Find each white blood cell.
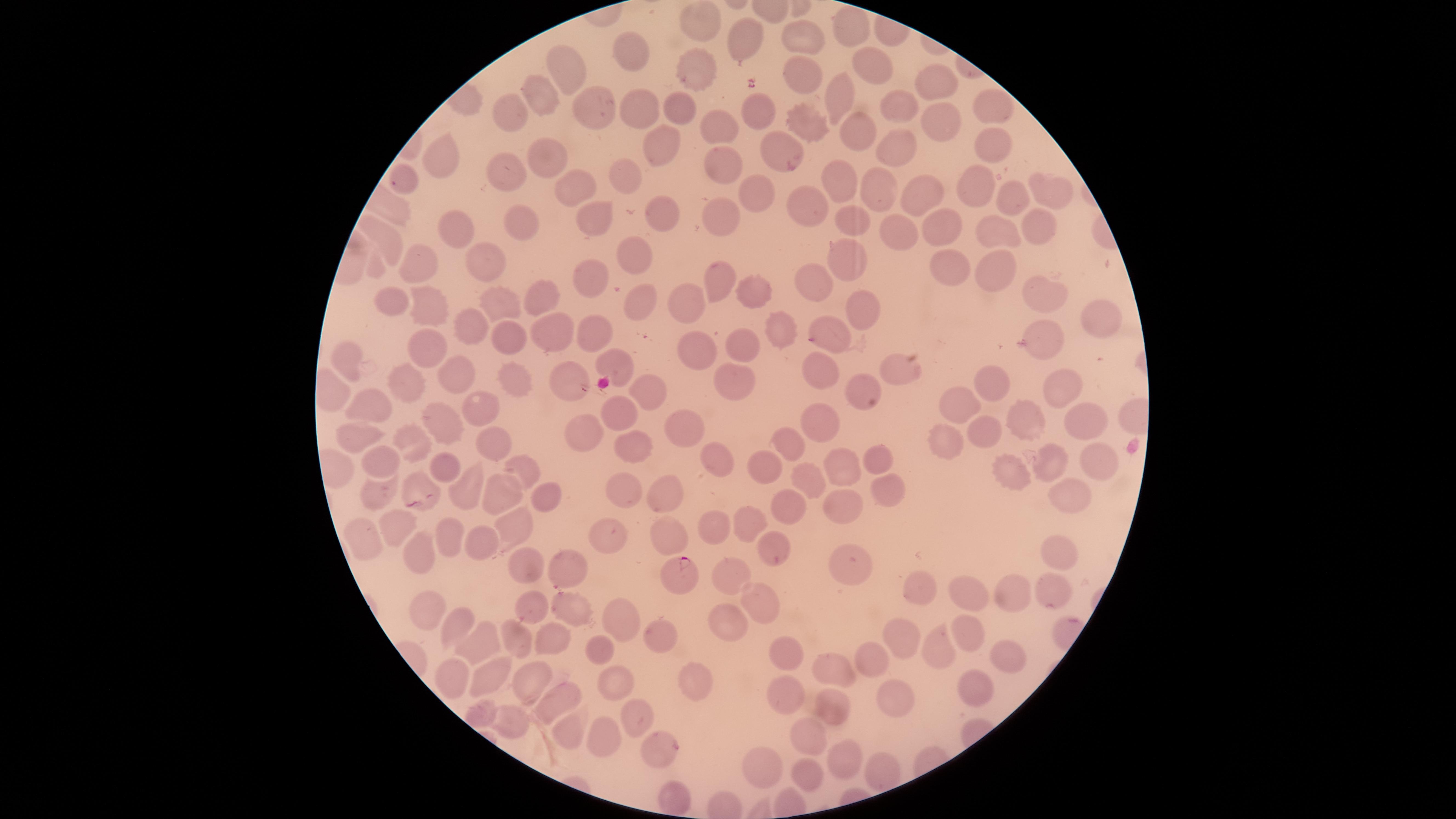

No white blood cells identified.

Approximate marker points as {x, y} in pixels.
Summary:
  - Parasitized red blood cells: {679, 573}
  - Uninfected red blood cells: {704, 20}, {856, 27}, {745, 38}, {808, 40}, {634, 46}, {871, 68}, {566, 69}, {696, 74}, {800, 79}, {940, 79}, {835, 97}, {541, 100}, {985, 104}, {637, 106}, {902, 106}, {663, 108}, {756, 109}, {595, 110}, {512, 111}, {942, 123}, {804, 124}, {854, 126}, {720, 128}, {987, 140}, {655, 146}, {779, 148}, {899, 152}, {547, 159}, {447, 160}, {506, 170}, {733, 170}, {841, 177}, {405, 181}, {620, 181}, {1050, 184}, {571, 186}, {876, 187}, {980, 187}, {913, 191}, {1013, 194}, {749, 195}, {806, 208}, {595, 209}, {656, 216}, {528, 221}, {720, 223}, {850, 223}, {1034, 223}, {455, 228}, {946, 229}, {907, 233}, {999, 233}, {385, 235}, {637, 249}, {477, 257}, {845, 262}, {951, 263}, {414, 264}, {991, 273}, {592, 275}, {716, 276}, {811, 281}, {755, 292}, {1044, 294}, {502, 296}, {549, 296}, {640, 299}, {397, 301}, {424, 303}, {688, 304}, {864, 309}, {1100, 318}, {776, 321}, {464, 327}, {596, 330}, {550, 333}, {1044, 333}, {837, 334}, {503, 336}, {704, 345}, {433, 346}, {744, 348}, {350, 361}, {616, 361}, {901, 368}, {821, 372}, {461, 375}, {736, 378}, {404, 381}, {512, 381}, {567, 381}, {996, 386}, {649, 388}, {860, 388}, {1061, 388}, {960, 404}, {377, 407}, {482, 411}, {624, 411}, {445, 416}, {822, 417}, {1025, 417}, {1088, 420}, {690, 423}, {586, 426}, {362, 436}, {492, 442}, {412, 444}, {633, 445}, {787, 445}, {716, 456}, {876, 456}, {1096, 463}, {382, 464}, {1047, 466}, {443, 468}, {521, 469}, {761, 470}, {842, 471}, {1013, 473}, {806, 484}, {414, 486}, {625, 489}, {887, 489}, {471, 490}, {672, 493}, {378, 496}, {1067, 498}, {501, 499}, {544, 499}, {842, 508}, {782, 509}, {750, 523}, {399, 525}, {711, 526}, {514, 530}, {610, 531}, {445, 534}, {668, 538}, {360, 541}, {480, 542}, {774, 552}, {420, 553}, {1049, 554}, {565, 563}, {518, 566}, {846, 570}, {733, 573}, {917, 588}, {972, 590}, {1052, 596}, {1016, 599}, {570, 601}, {759, 604}, {530, 605}, {429, 611}, {614, 618}, {729, 624}, {456, 625}, {968, 630}, {661, 633}, {903, 634}, {547, 636}, {482, 639}, {516, 645}, {937, 647}, {601, 649}, {786, 649}, {1010, 656}, {839, 667}, {878, 668}, {452, 678}, {489, 678}, {528, 679}, {697, 682}, {614, 684}, {978, 685}, {785, 694}, {558, 698}, {897, 701}, {831, 707}, {478, 714}, {639, 716}, {509, 721}, {603, 729}, {566, 735}, {809, 737}, {665, 752}, {841, 755}, {878, 768}, {763, 770}, {808, 772}, {672, 792}
  - Visible region: circular
  - Species: Plasmodium falciparum
  - Preparation: thin smear of blood
  - Presence: malaria parasites seen
  - Stain: Giemsa
  - Field of view: single
  - Capture: smartphone photograph through the microscope eyepiece
  - Image size: 1456×819 pixels